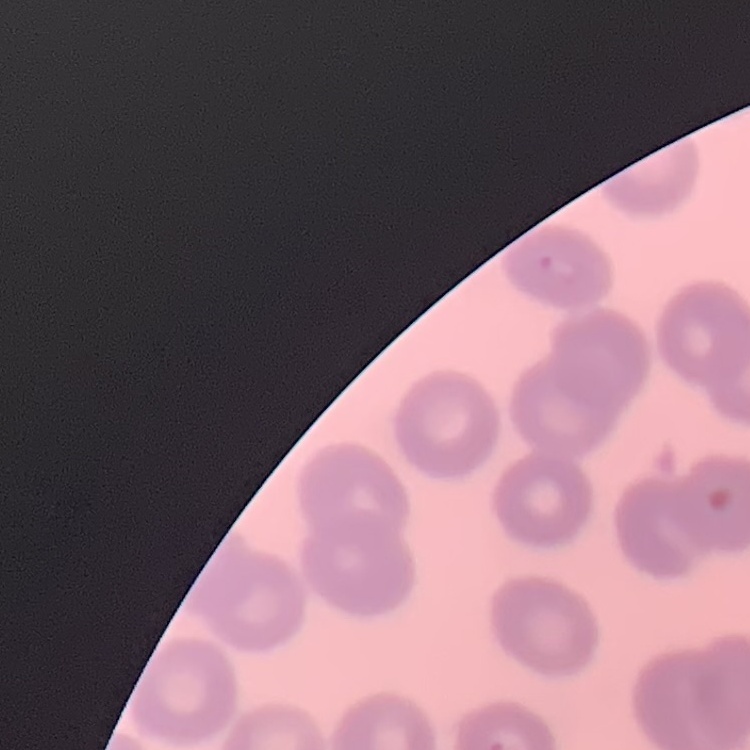

{
  "erythrocyte_morphology": "no rouleaux formation",
  "image_type": "one tile cut from a larger photomicrograph",
  "stain": "Field's or Giemsa",
  "preparation": "thin blood film"
}